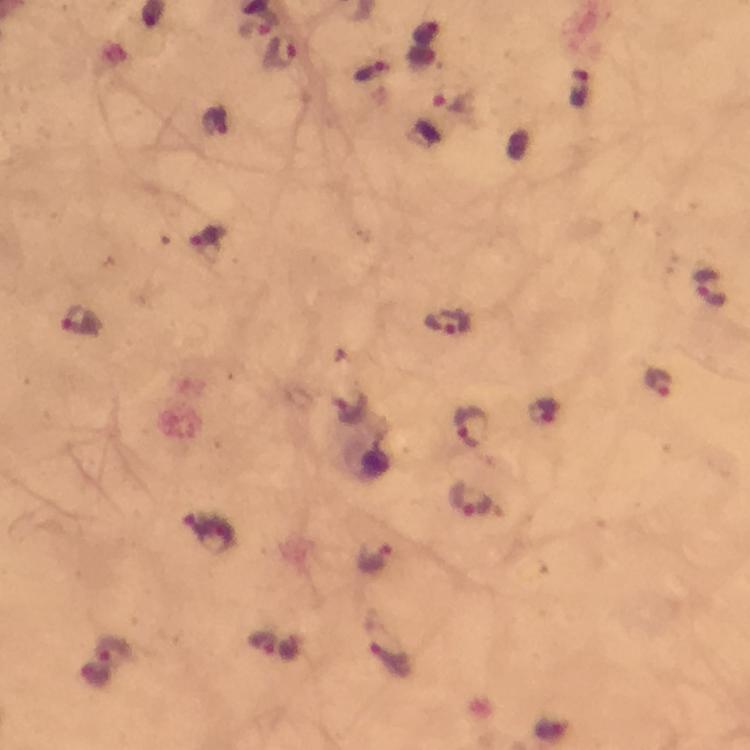
malaria parasite locations = approximate centers as (x, y) in pixels: (255, 30), (284, 55), (454, 104), (217, 123), (712, 288), (82, 321), (445, 321), (658, 384), (471, 428), (468, 499), (378, 559), (261, 643)
immersion oil = applied
context = from a malaria diagnostic workup
preparation = thick blood smear
stain = Giemsa
magnification = 100x
capture = smartphone photograph through a microscope
cropped from = a single field of view
image size = 750×750 pixels